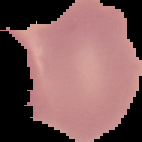
{
  "preparation": "thin blood film",
  "image_size": "142×142 pixels",
  "malaria_status": "uninfected",
  "image_type": "segmented cell region on a black background"
}